Comment on the morphology of the erythrocytes.
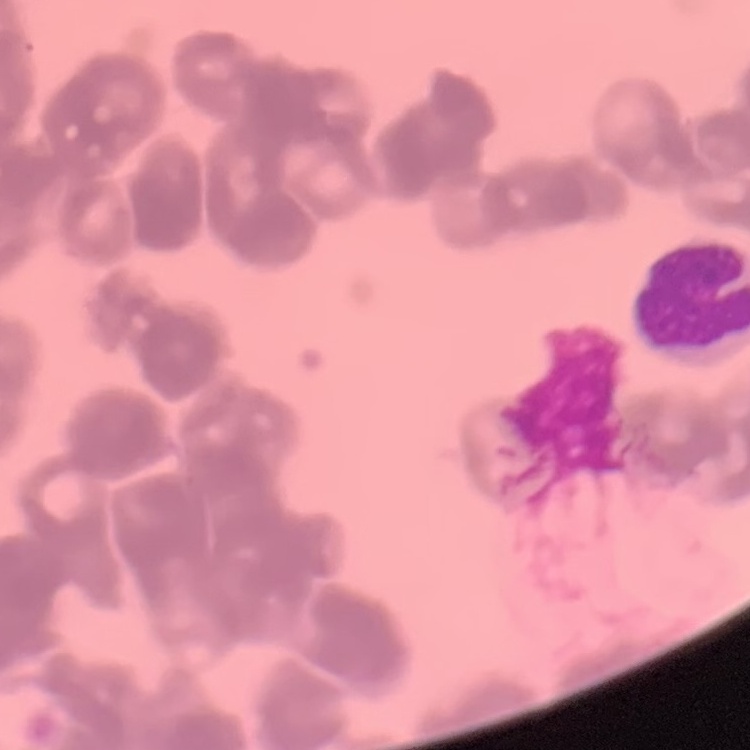

Rouleaux formation.

preparation: thin blood film
image_type: square crop of a larger photomicrograph
stain: Field's or Giemsa